Describe the morphology of the erythrocytes.
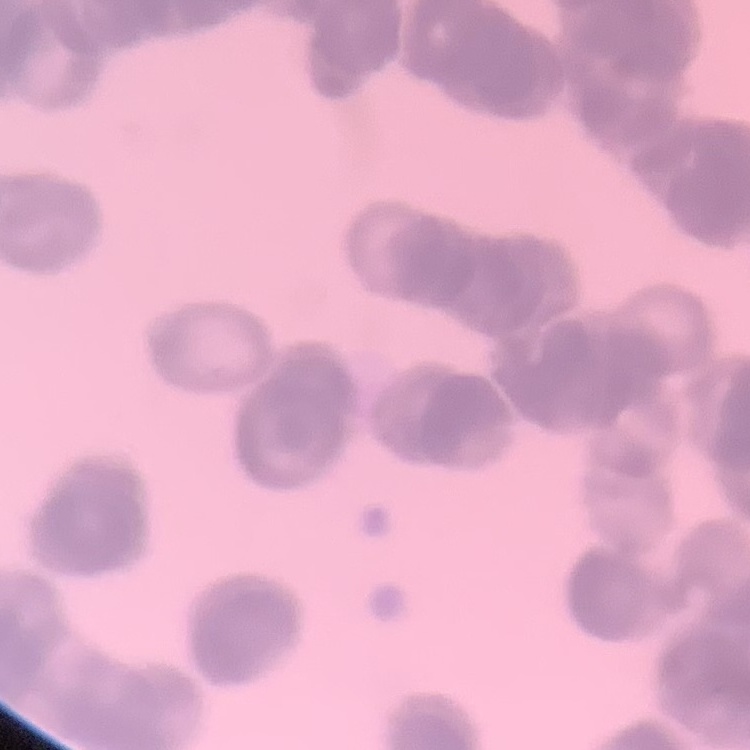
Rouleaux formation.

Summary:
  - Image type: one tile cut from a larger photomicrograph
  - Preparation: thin blood film
  - Stain: Field's or Giemsa